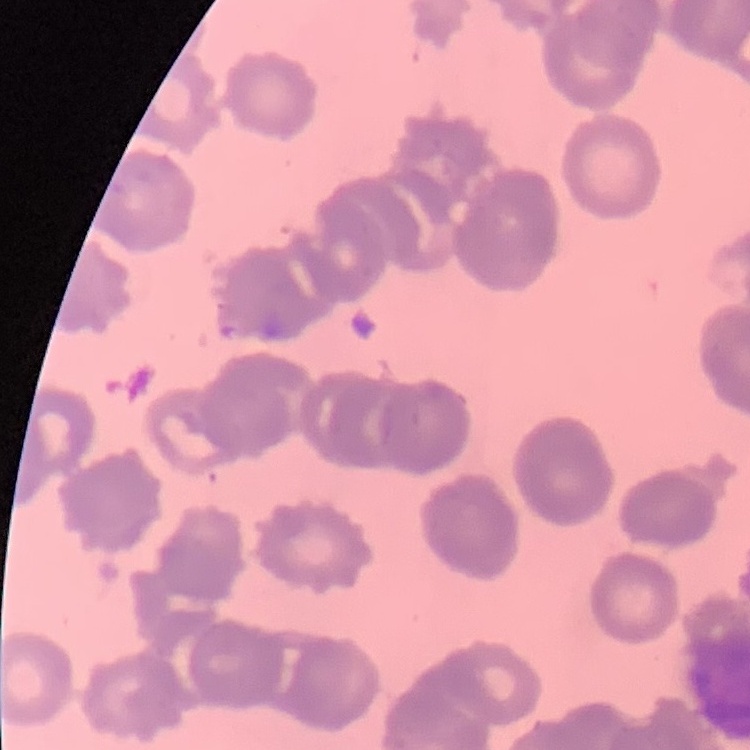

Summary:
  - Red blood cell morphology: rouleaux formation
  - Stain: Field's or Giemsa
  - Preparation: thin peripheral smear
  - Image type: one tile cut from a larger photomicrograph